Identify the preparation type.
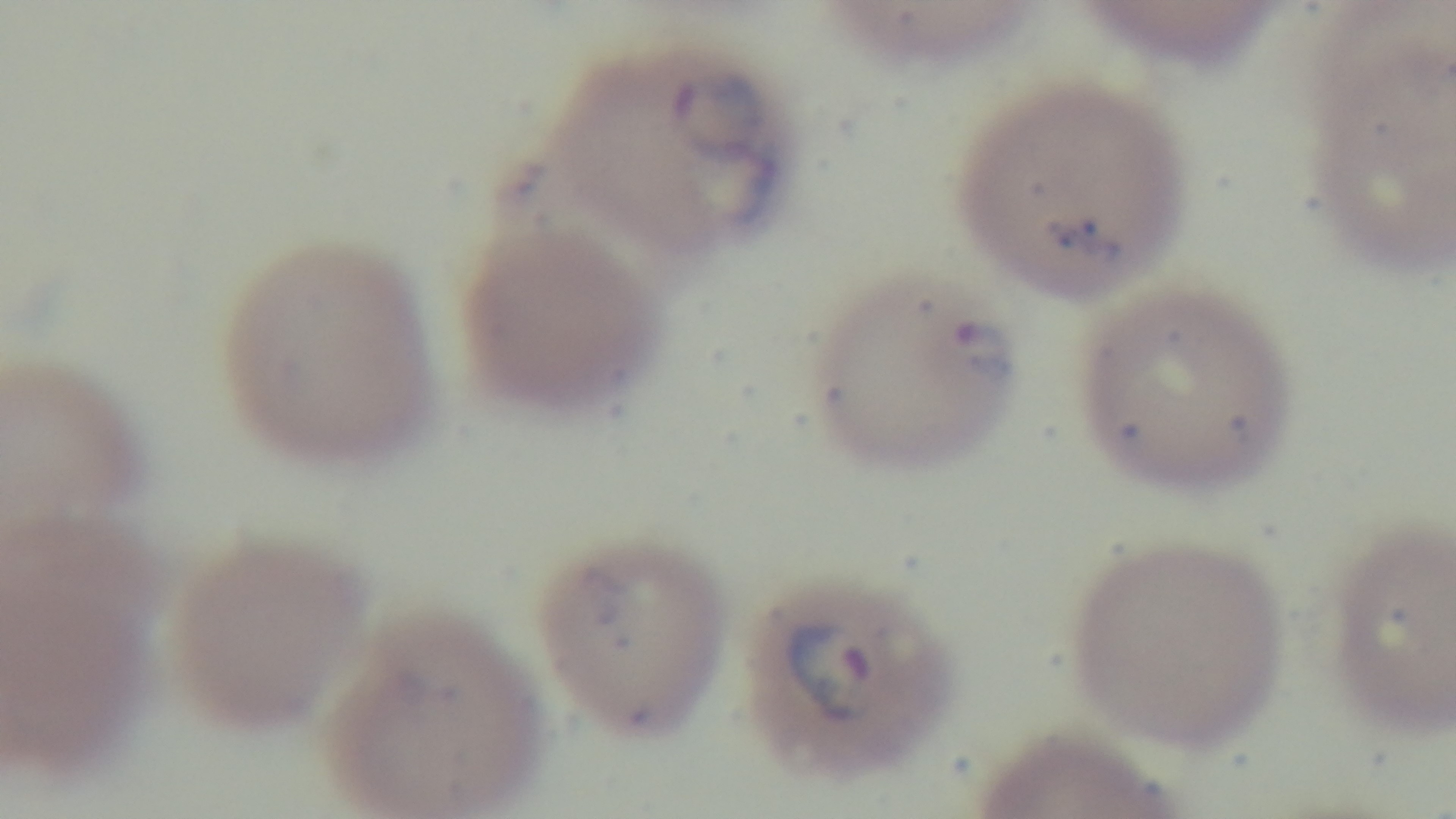

It is a thin blood film.

Summary:
  - Field of view: single
  - Objective: 100x oil immersion
  - Stain: Giemsa
  - Capture: mounted 4K digital camera
  - Malaria status: infected
  - Modality: light microscopy